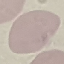
Summary:
  - Result: no malaria parasites seen
  - Stain: Giemsa
  - Preparation: thin blood smear
  - Image type: automatically extracted cell patch, resized to 64 × 64 pixels
  - Capture: smartphone camera at the microscope eyepiece